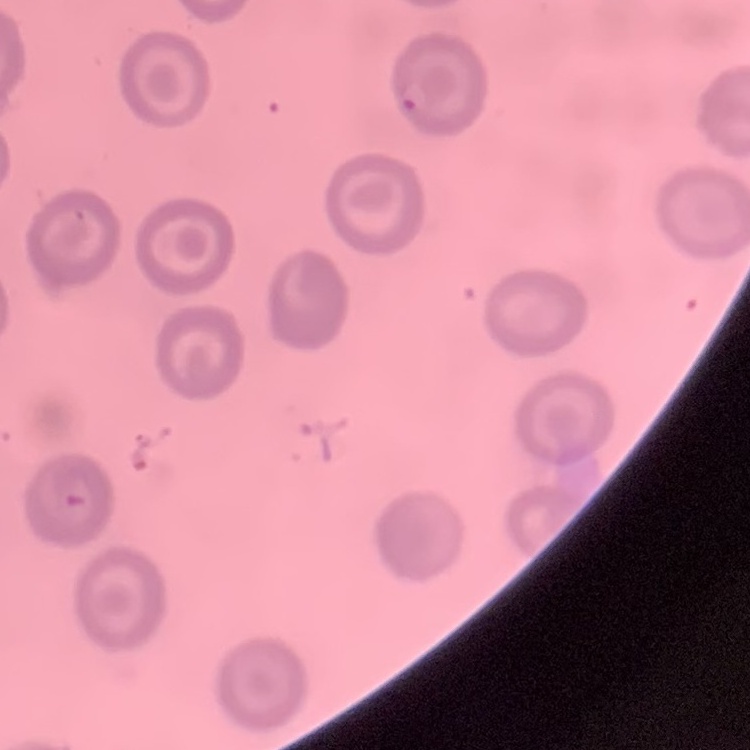
Summary:
  - Erythrocyte morphology: no rouleaux formation
  - Stain: Field's or Giemsa
  - Preparation: thin blood film
  - Image type: square crop of a larger photomicrograph